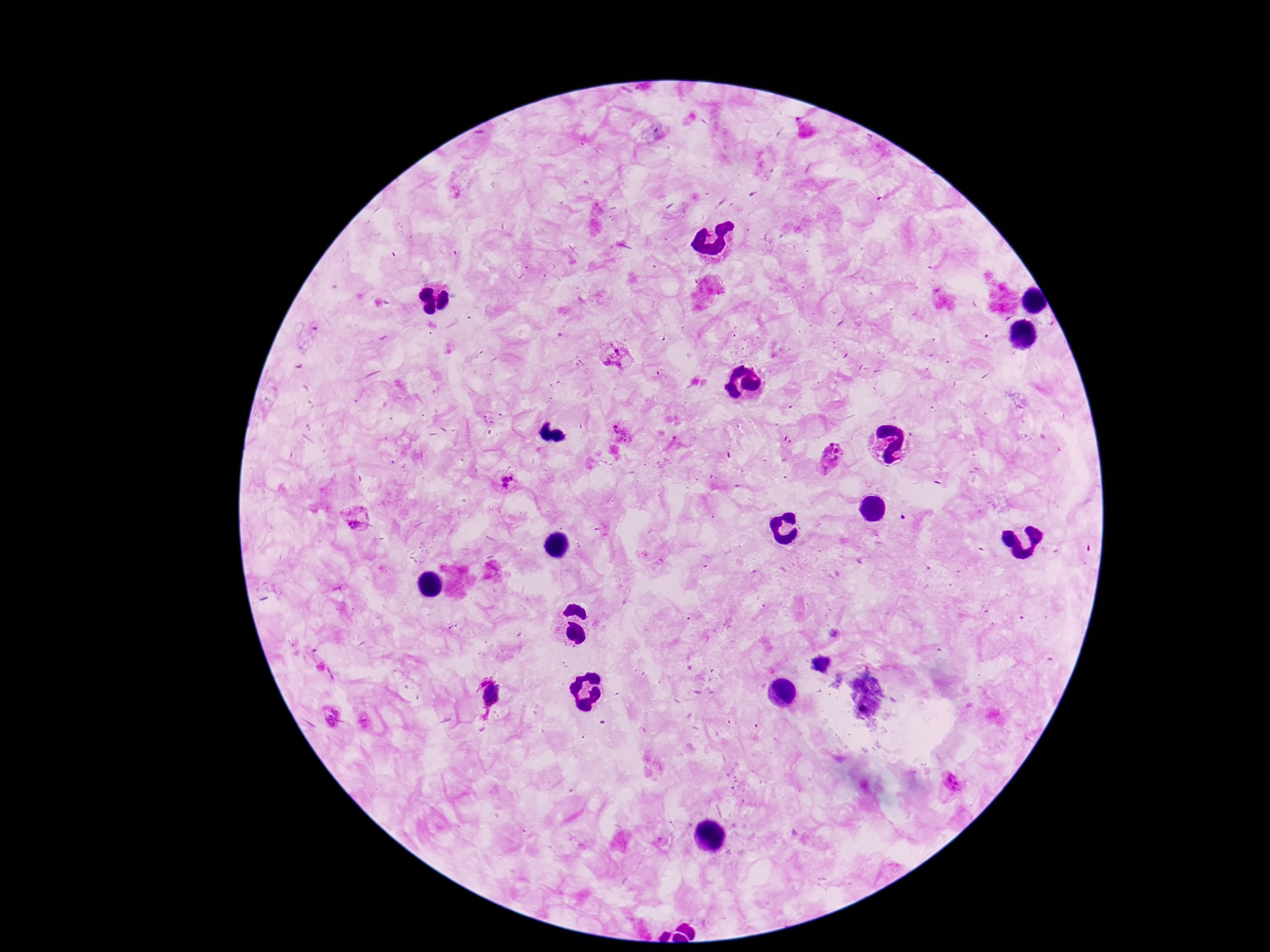

stain: Giemsa
preparation: thick blood smear
field_of_view: single
plasmodium_parasite_locations: 'approximate centers as (x, y) in pixels: (615, 355), (621, 430), (832, 457), (506, 481), (357, 515), (835, 635), (490, 697), (329, 715), (951, 782)'
capture: smartphone camera through the microscope eyepiece
magnification: 100x
patient_malaria_status: infected
image_size: 1270×952 pixels